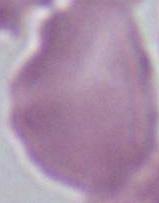
{
  "magnification": "1000x",
  "modality": "micrograph",
  "identification": "red blood cell"
}